Identify the parasite.
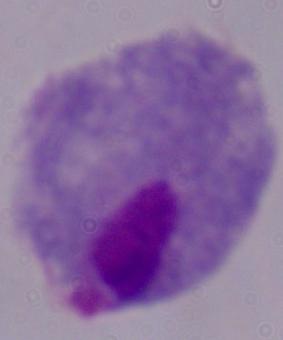
A trichomonad.

Summary:
  - Modality: photomicrograph
  - Magnification: 1000x